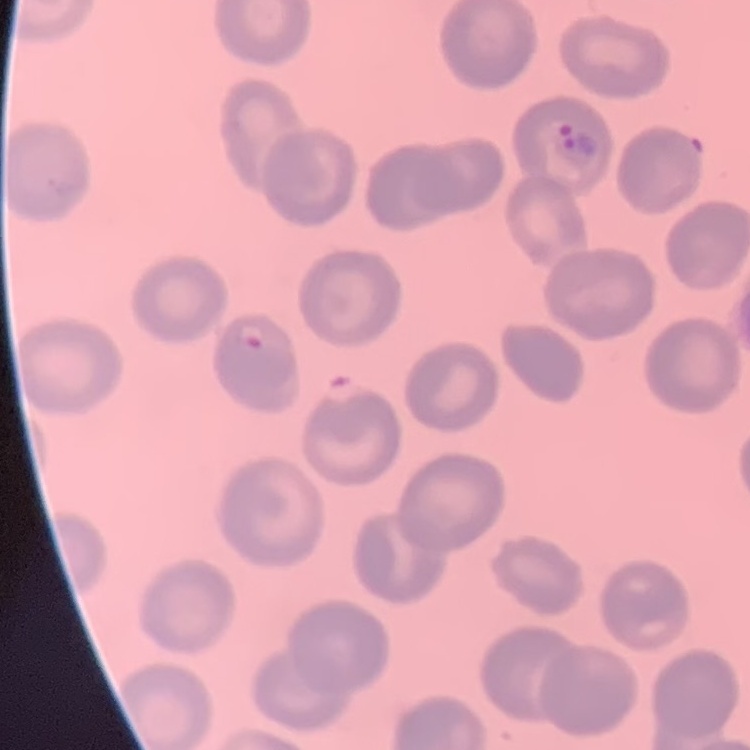
The erythrocytes exhibit no rouleaux formation. Square crop of a larger photomicrograph. Thin blood film. Stained with either Field's or Giemsa.